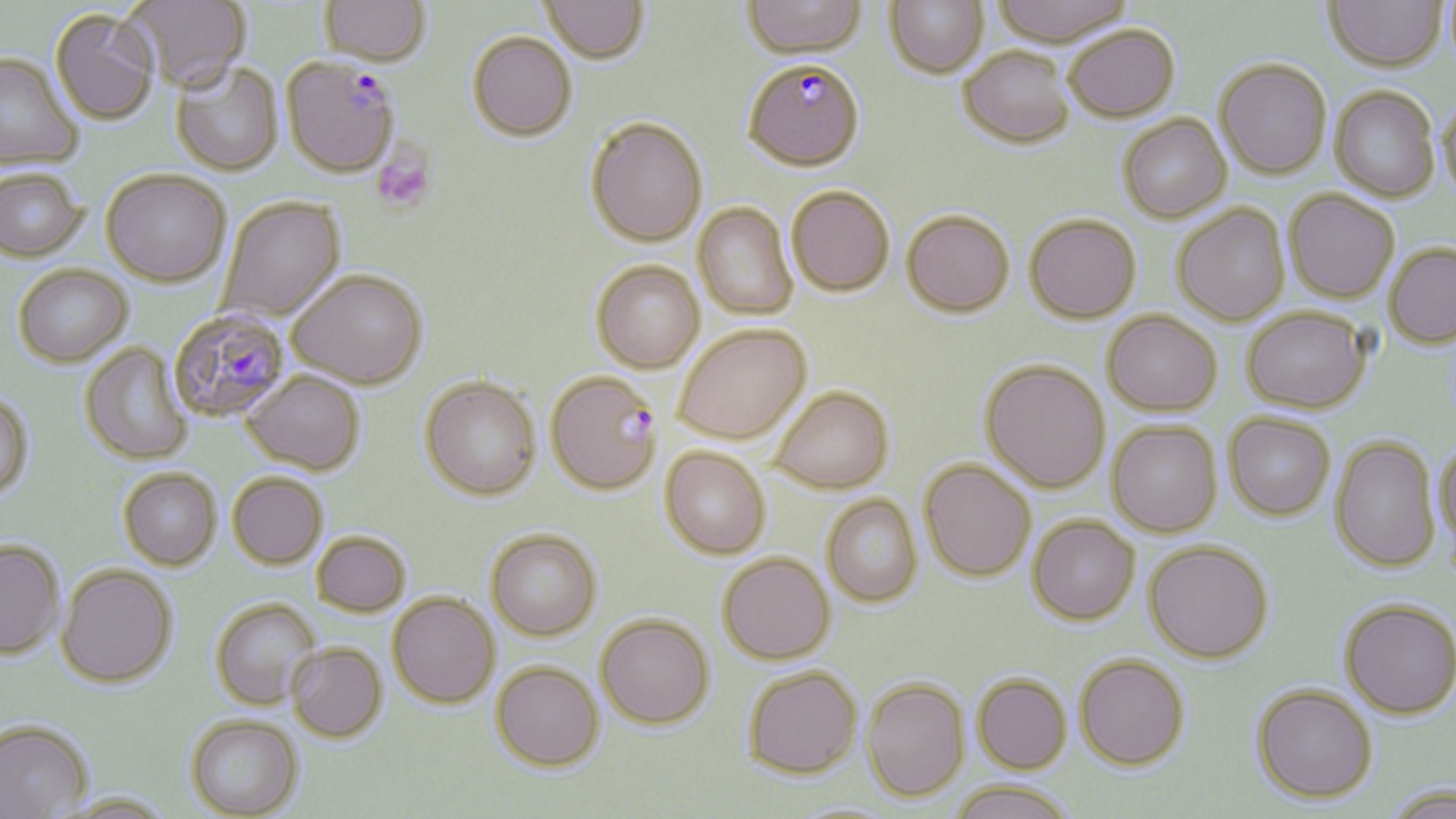
{
  "slide_level_diagnosis": "Plasmodium falciparum",
  "image_size": "1456×819 pixels",
  "magnification": "1000x",
  "modality": "optical microscopy",
  "uninfected_red_blood_cell_locations": "approximate bounding boxes as [x1, y1, x2, y2] in pixels: [124, 0, 252, 95], [319, 0, 430, 67], [539, 0, 649, 66], [742, 0, 867, 58], [884, 0, 988, 78], [991, 0, 1131, 46], [1441, 0, 1456, 69], [1324, 1, 1446, 70], [50, 9, 160, 127], [1064, 25, 1180, 122], [467, 33, 577, 143], [958, 46, 1075, 148], [0, 53, 82, 170], [1214, 58, 1332, 179], [170, 63, 284, 178], [1330, 86, 1440, 201], [1437, 97, 1456, 202], [1118, 113, 1231, 223], [585, 119, 707, 248], [0, 171, 86, 263], [101, 173, 231, 289], [787, 186, 895, 296], [1284, 190, 1400, 303], [218, 197, 347, 324], [693, 203, 799, 320], [1171, 204, 1290, 325], [901, 210, 1015, 317], [1024, 213, 1141, 323], [1384, 242, 1456, 348], [591, 262, 705, 374], [13, 266, 134, 370], [287, 272, 429, 391], [1241, 306, 1371, 412], [1102, 310, 1222, 415], [674, 325, 811, 444], [80, 343, 195, 466], [980, 360, 1110, 493], [240, 372, 365, 477], [419, 379, 542, 502], [769, 386, 894, 494], [0, 390, 34, 505], [1224, 412, 1336, 520], [1107, 421, 1223, 537], [1330, 436, 1440, 572], [1434, 441, 1456, 556], [660, 447, 771, 559], [919, 459, 1035, 581], [118, 471, 221, 572], [228, 475, 328, 571], [821, 494, 923, 606], [1028, 515, 1140, 624], [485, 530, 601, 642], [312, 533, 411, 618], [1143, 540, 1273, 663], [0, 541, 65, 662], [717, 553, 836, 664], [56, 567, 177, 690], [387, 594, 499, 710], [1339, 599, 1456, 718], [210, 600, 321, 711], [595, 614, 715, 731], [286, 644, 388, 744], [1074, 654, 1190, 769], [490, 664, 605, 774], [744, 666, 863, 779], [972, 674, 1072, 773], [861, 677, 970, 801], [1251, 683, 1377, 802], [185, 717, 304, 819], [0, 723, 93, 819], [950, 779, 1076, 819], [1382, 783, 1456, 818], [56, 795, 176, 819], [786, 801, 904, 819]",
  "plasmodium_falciparum_infected_red_blood_cell_locations": "approximate bounding boxes as [x1, y1, x2, y2] in pixels: [281, 57, 401, 180], [743, 58, 865, 170], [168, 311, 291, 424], [546, 373, 662, 496]",
  "field_of_view": "one of a larger specimen",
  "platelet_locations": "approximate bounding boxes as [x1, y1, x2, y2] in pixels: [372, 146, 436, 213]",
  "preparation": "thin blood smear",
  "stain": "May-Grünwald-Giemsa"
}